Name the parasite shown.
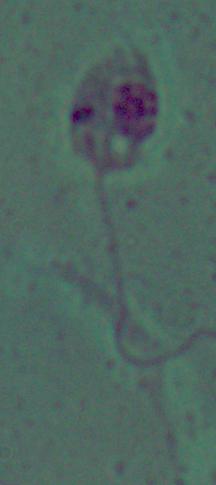

This is Leishmania.

Photomicrograph. 1000x magnification.